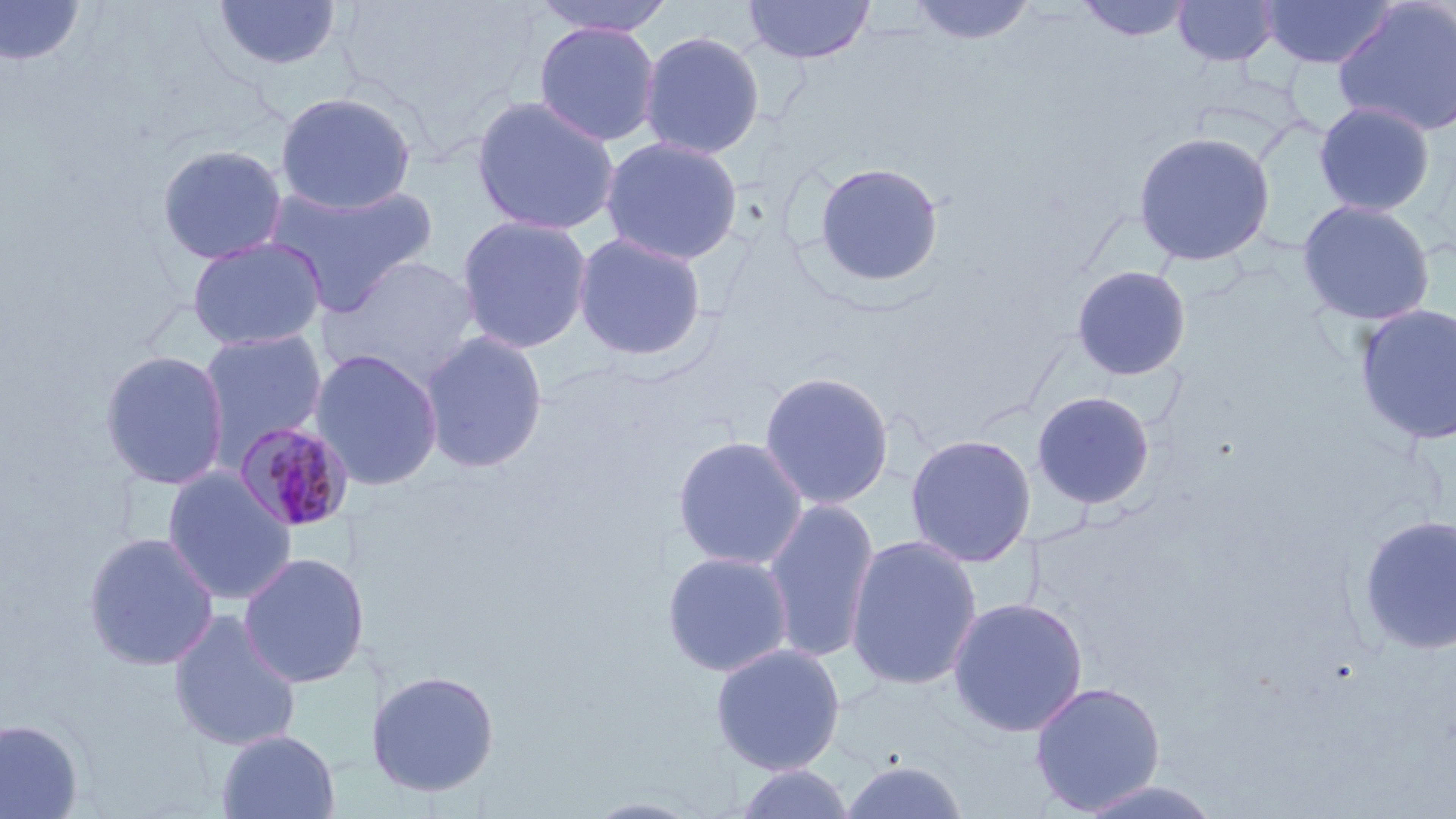 Approximate bounding boxes as (x1,y1)-(x2,y2) corner pairs in pixels. Plasmodium malariae-infected red blood cell locations: (231,420)-(356,534). Uninfected red blood cell locations: (527,0)-(678,37), (741,0)-(876,64), (906,0)-(1039,46), (1076,0)-(1197,43), (1172,0)-(1282,67), (1258,0)-(1398,69), (0,1)-(86,67), (210,1)-(344,73), (1333,1)-(1456,137), (532,21)-(662,147), (638,29)-(766,160), (274,91)-(418,215), (469,94)-(621,237), (1313,100)-(1436,217), (1132,130)-(1276,267), (600,136)-(743,266), (155,143)-(289,266), (813,161)-(944,288), (264,177)-(439,316), (1296,199)-(1436,326), (455,214)-(594,354), (572,231)-(709,361), (186,235)-(328,351), (320,254)-(484,387), (1070,264)-(1192,381), (1352,302)-(1456,447), (196,328)-(329,460), (419,331)-(549,474), (309,348)-(445,491), (98,349)-(231,491), (758,370)-(895,510), (1030,390)-(1156,510), (904,433)-(1037,568), (671,434)-(809,570), (162,467)-(298,606), (761,498)-(880,664), (1357,514)-(1456,656), (82,532)-(220,671), (844,534)-(983,692), (661,550)-(795,678), (238,552)-(371,688), (946,596)-(1089,738), (168,610)-(303,752), (710,643)-(846,775), (365,669)-(500,798), (1028,680)-(1166,815), (0,717)-(84,818), (215,728)-(340,819), (839,758)-(969,819), (731,763)-(858,819), (1072,779)-(1227,819), (582,796)-(707,818). Slide-level diagnosis: Plasmodium malariae. Thin blood film. 1000x magnification. Optical microscopy. Image is 1456×819 pixels. One field of a larger specimen. May-Grünwald-Giemsa stain.